Identify the cell.
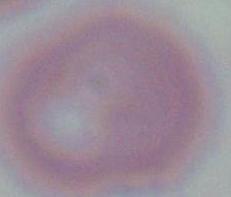

This is an erythrocyte.

Summary:
  - Modality: photomicrograph
  - Magnification: 1000x